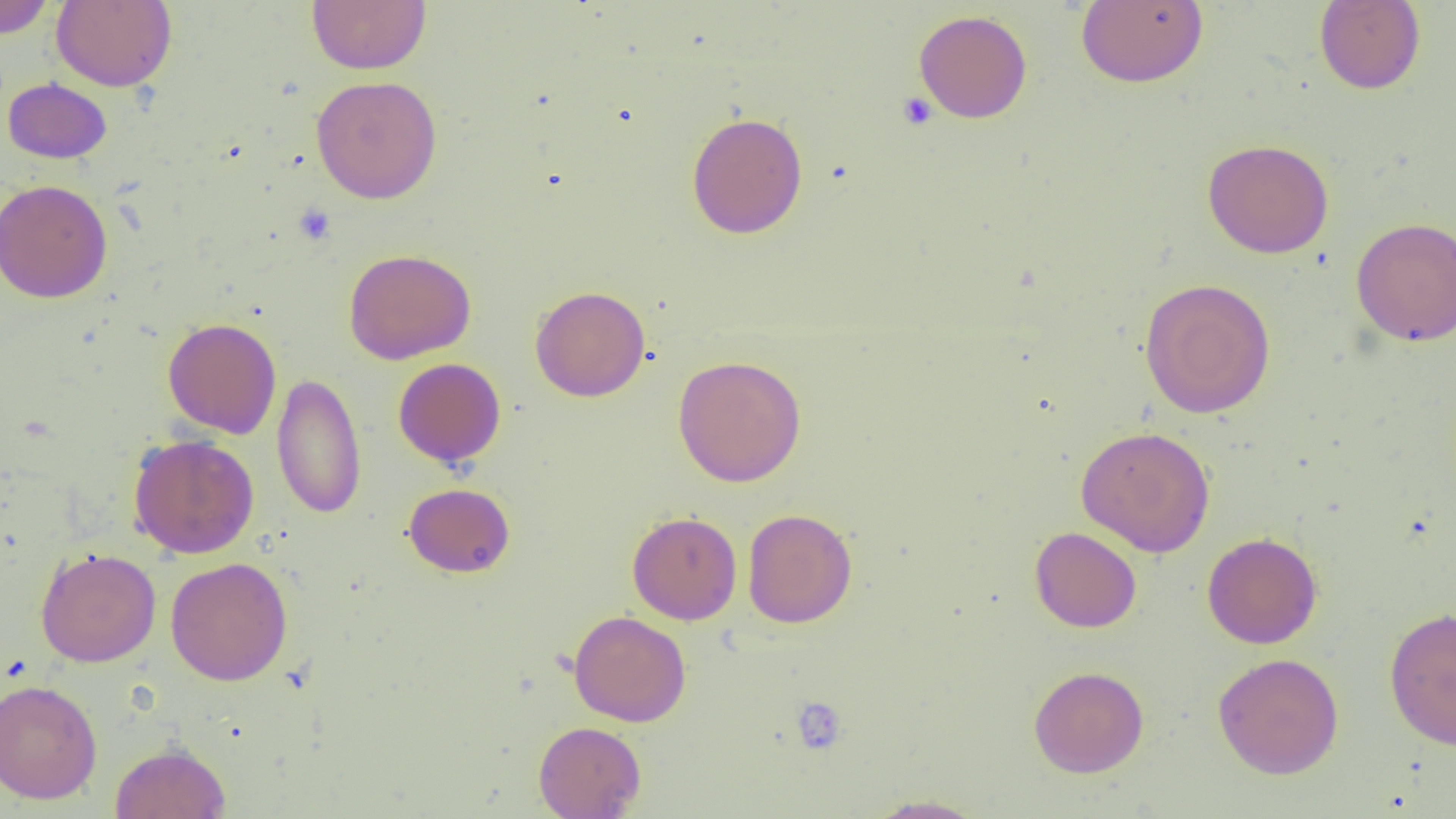

{
  "slide_level_diagnosis": "no evidence of blood parasites",
  "platelet_locations": "approximate bounding boxes as (x1, y1, x2, y2) in pixels: (897, 91, 938, 131), (292, 204, 335, 245), (790, 696, 848, 756)",
  "field_of_view": "one of a larger specimen",
  "preparation": "thin blood smear",
  "modality": "light microscopy",
  "image_size": "1456×819 pixels",
  "magnification": "1000x",
  "uninfected_red_blood_cell_locations": "approximate bounding boxes as (x1, y1, x2, y2) in pixels: (0, 0, 56, 39), (52, 0, 177, 91), (306, 0, 431, 74), (1076, 0, 1209, 88), (1314, 1, 1425, 95), (914, 9, 1032, 123), (311, 75, 442, 203), (2, 78, 112, 163), (686, 112, 808, 239), (1202, 139, 1334, 259), (0, 179, 113, 303), (1350, 217, 1456, 345), (343, 248, 476, 365), (1139, 278, 1276, 419), (530, 285, 650, 402), (162, 317, 282, 439), (672, 354, 807, 487), (393, 358, 506, 467), (271, 372, 366, 519), (1075, 425, 1215, 557), (128, 433, 259, 558), (403, 482, 516, 577), (742, 508, 857, 628), (627, 511, 742, 625), (1030, 526, 1142, 633), (1202, 532, 1322, 649), (35, 547, 162, 667), (165, 557, 293, 686), (1384, 606, 1456, 751), (568, 610, 691, 727), (1212, 652, 1344, 779), (1028, 665, 1149, 778), (0, 679, 102, 804), (534, 721, 646, 819), (110, 741, 231, 819), (863, 794, 989, 818)"
}